Assess this cell for malaria.
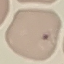
Uninfected.

Summary:
  - Stain: Giemsa
  - Preparation: thin smear
  - Capture: smartphone through the microscope eyepiece
  - Image type: cell patch, automatically extracted from a larger field of view and resized to 64 × 64 pixels